Identify the parasite.
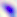

Toxoplasma gondii.

modality = photomicrograph
magnification = 400x